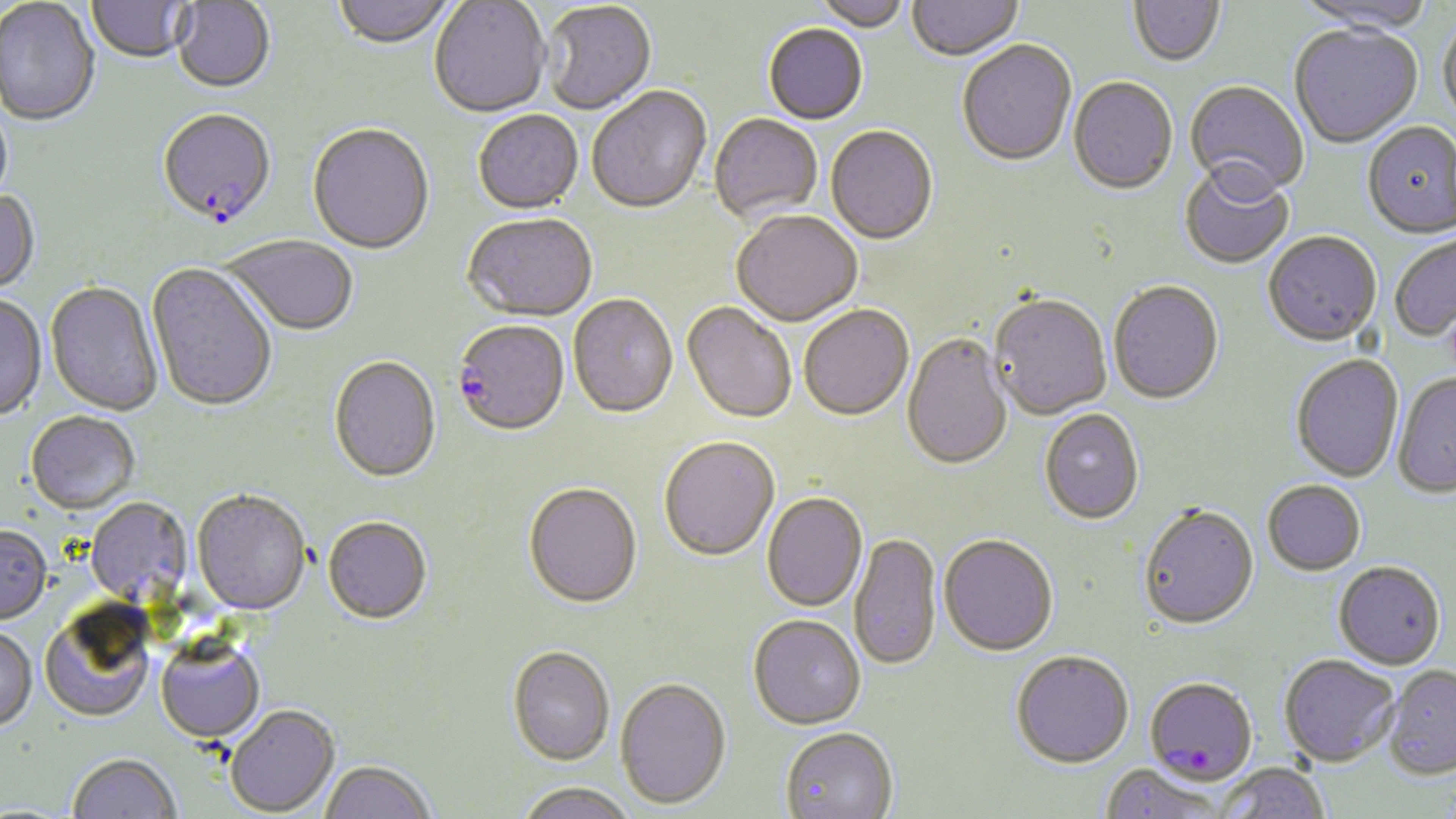

slide-level diagnosis = Plasmodium falciparum
modality = optical microscopy
magnification = 1000x
stain = May-Grünwald-Giemsa
image size = 1456×819 pixels
Plasmodium falciparum-infected red blood cell locations = approximate bounding boxes as (x1,y1)-(x2,y2) corner pairs in pixels: (157,111)-(277,232), (452,322)-(569,439), (1144,677)-(1257,786)
uninfected red blood cell locations = approximate bounding boxes as (x1,y1)-(x2,y2) corner pairs in pixels: (332,0)-(457,51), (811,0)-(910,33), (1292,0)-(1437,36), (0,1)-(100,128), (87,1)-(193,65), (429,1)-(551,120), (907,1)-(1024,64), (1128,1)-(1226,69), (170,2)-(275,95), (540,4)-(656,116), (1438,17)-(1456,131), (763,25)-(868,126), (1289,25)-(1422,150), (957,42)-(1077,169), (1068,79)-(1178,197), (1184,81)-(1309,204), (587,88)-(712,217), (473,112)-(584,216), (709,115)-(823,224), (1362,123)-(1456,241), (307,125)-(434,256), (826,127)-(938,247), (1179,167)-(1295,270), (0,191)-(41,297), (731,213)-(862,329), (463,215)-(597,324), (1389,231)-(1456,343), (1263,234)-(1381,348), (223,236)-(358,338), (146,264)-(277,415), (45,282)-(163,416), (1108,283)-(1224,406), (0,295)-(46,422), (568,296)-(678,420), (989,297)-(1111,422), (682,303)-(796,425), (799,307)-(913,422), (901,335)-(1013,472), (1291,354)-(1404,483), (328,357)-(441,485), (1392,372)-(1456,499), (1039,410)-(1144,527), (25,412)-(140,516), (659,439)-(779,563), (1262,481)-(1366,576), (523,485)-(643,611), (192,492)-(311,615), (762,494)-(867,613), (86,497)-(192,606), (1138,506)-(1259,632), (322,518)-(432,626), (0,525)-(51,626), (850,534)-(942,674), (939,536)-(1058,658), (1333,561)-(1445,669), (40,606)-(154,723), (748,618)-(866,732), (0,628)-(37,733), (155,637)-(265,743), (507,647)-(615,767), (1011,652)-(1133,770), (1279,654)-(1400,766), (1383,665)-(1456,779), (615,679)-(731,810), (226,706)-(339,817), (780,729)-(898,819), (67,754)-(181,819), (320,761)-(434,819), (1216,762)-(1331,819), (1100,766)-(1227,818), (515,783)-(639,819)
preparation = thin blood film
field of view = one of a larger specimen